Assess this cell for malaria.
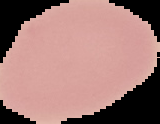
Uninfected.

Summary:
  - Image type: cell region segmented out of the field of view; surrounding area masked to black
  - Image size: 160×124 pixels
  - Preparation: thin blood film